Give the position of every leukocyte visible.
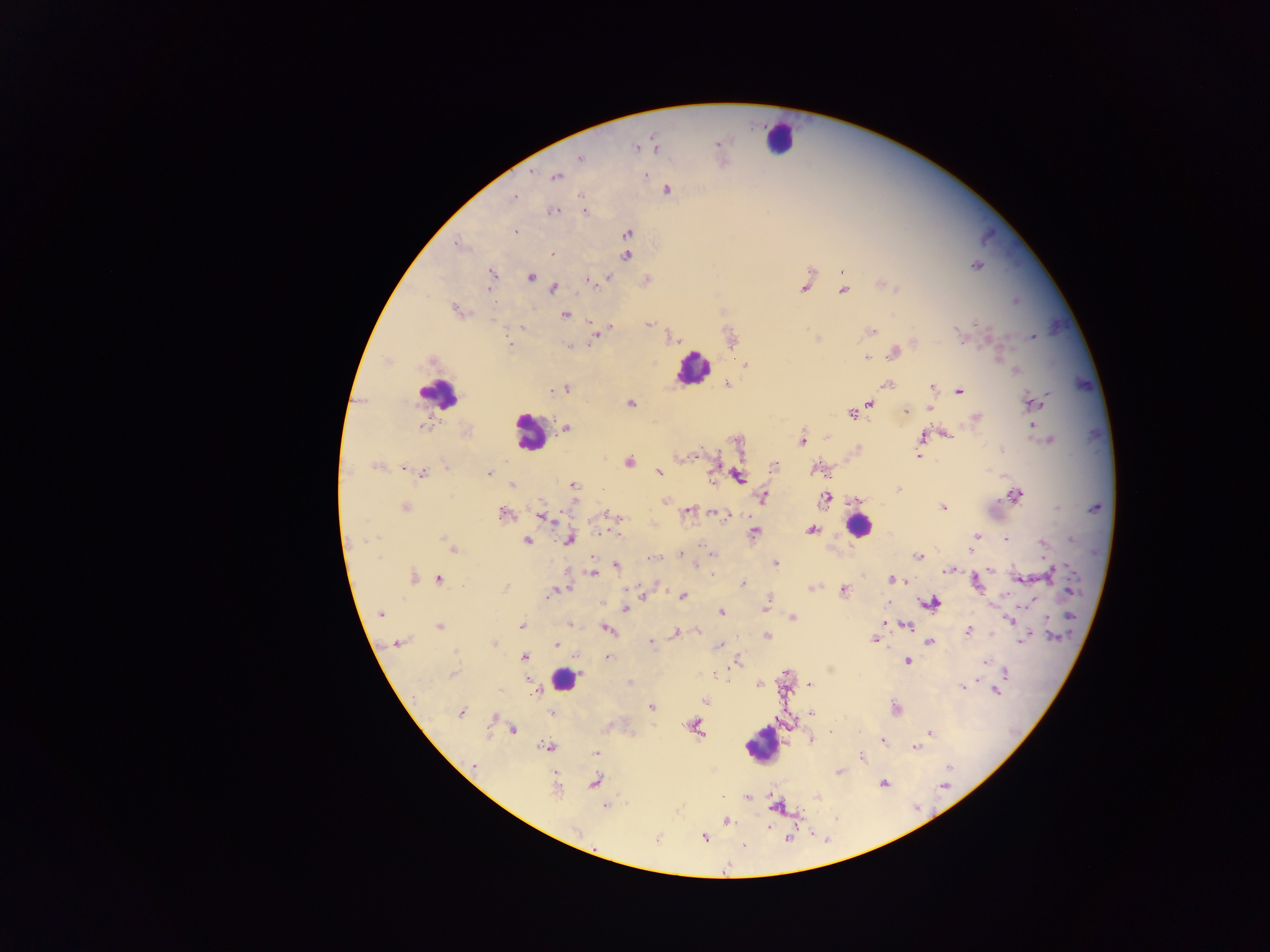

Approximate centers as [x, y] in pixels.
Leukocytes: [779, 137], [693, 368], [439, 393], [529, 432], [858, 526], [564, 679], [763, 746].

Summary:
  - Plasmodium parasite locations: [718, 143], [654, 145], [636, 147], [579, 157], [555, 176], [666, 189], [582, 195], [513, 197], [583, 210], [552, 211], [514, 232], [626, 234], [458, 244], [553, 253], [626, 255], [976, 265], [841, 272], [492, 275], [530, 276], [607, 277], [588, 281], [645, 281], [882, 284], [489, 286], [805, 286], [553, 288], [842, 290], [458, 310], [565, 313], [592, 321], [648, 324], [522, 327], [607, 327], [869, 331], [957, 332], [596, 336], [1033, 336], [671, 337], [730, 337], [817, 338], [508, 343], [914, 343], [568, 345], [894, 351], [867, 358], [432, 359], [745, 365], [1015, 370], [726, 383], [887, 384], [932, 386], [566, 388], [560, 389], [551, 390], [957, 391], [630, 402], [868, 402], [1031, 403], [930, 408], [906, 411], [852, 414], [975, 417], [423, 426], [1034, 426], [565, 428], [466, 431], [943, 434], [826, 436], [923, 437], [736, 439], [801, 440], [1049, 440], [859, 448], [695, 454], [918, 456], [680, 457], [628, 462], [775, 465], [376, 466], [446, 467], [402, 468], [817, 468], [658, 471], [488, 472], [422, 474], [737, 476], [573, 485], [511, 486], [898, 488], [1016, 495], [762, 497], [826, 498], [664, 501], [858, 501], [405, 507], [942, 507], [687, 510], [711, 512], [504, 513], [607, 513], [727, 515], [544, 516], [811, 530], [755, 531], [600, 533], [976, 537], [1004, 538], [568, 539], [527, 541], [1042, 543], [452, 547], [971, 551], [680, 552], [711, 552], [919, 556], [657, 557], [775, 564], [695, 565], [615, 566], [951, 569], [989, 570], [591, 572], [1048, 573], [413, 577], [438, 578], [1019, 578], [891, 579], [906, 581], [741, 583], [976, 583], [505, 587], [812, 587], [844, 590], [1069, 591], [551, 593], [642, 594], [682, 596], [931, 603], [764, 606], [625, 608], [380, 613], [719, 613], [791, 617], [1010, 620], [885, 623], [568, 624], [906, 625], [440, 626], [522, 626], [606, 629], [697, 630], [967, 631], [676, 632], [767, 636], [1024, 638], [874, 640], [930, 641], [651, 642], [398, 643], [494, 644], [556, 644], [717, 646], [524, 657], [607, 657], [906, 661], [735, 662], [985, 662], [1006, 672], [453, 674], [528, 680], [630, 683], [758, 684], [809, 684], [962, 686], [996, 691], [535, 693], [704, 700], [651, 707], [894, 708], [811, 711], [461, 712], [551, 713], [495, 718], [694, 725], [511, 730], [930, 732], [881, 739], [810, 740], [548, 746], [914, 747], [595, 754], [861, 756], [473, 766], [838, 772], [595, 781], [884, 783], [556, 787], [818, 795], [747, 796], [605, 805], [776, 805], [725, 820], [768, 826], [703, 836], [656, 838], [789, 839], [743, 845]
  - Country: Ghana
  - Preparation: thick blood smear
  - Field of view: single
  - Capture: mobile-phone photograph through a microscope
  - Image size: 1270×952 pixels